Classify this cell by malaria status.
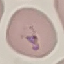

Parasitized.

Photographed with a smartphone camera at the microscope eyepiece. Cell patch, automatically extracted from a larger field of view and resized to 64 × 64 pixels. Giemsa stain. Thin blood smear.